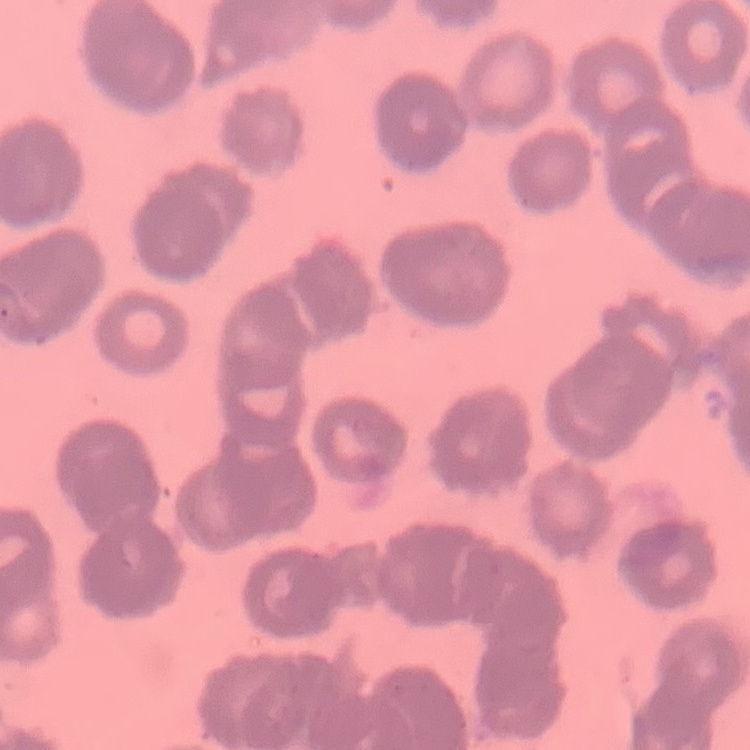

The red blood cells exhibit rouleaux formation. Thin blood smear. Square crop of a larger photomicrograph. Stained with either Field's or Giemsa.